Classify this cell by malaria status.
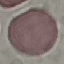
It is uninfected.

Summary:
  - Stain: Giemsa
  - Capture: smartphone camera at the microscope eyepiece
  - Image type: automatically extracted cell patch, resized to 64 × 64 pixels
  - Preparation: thin smear